Comment on the background quality.
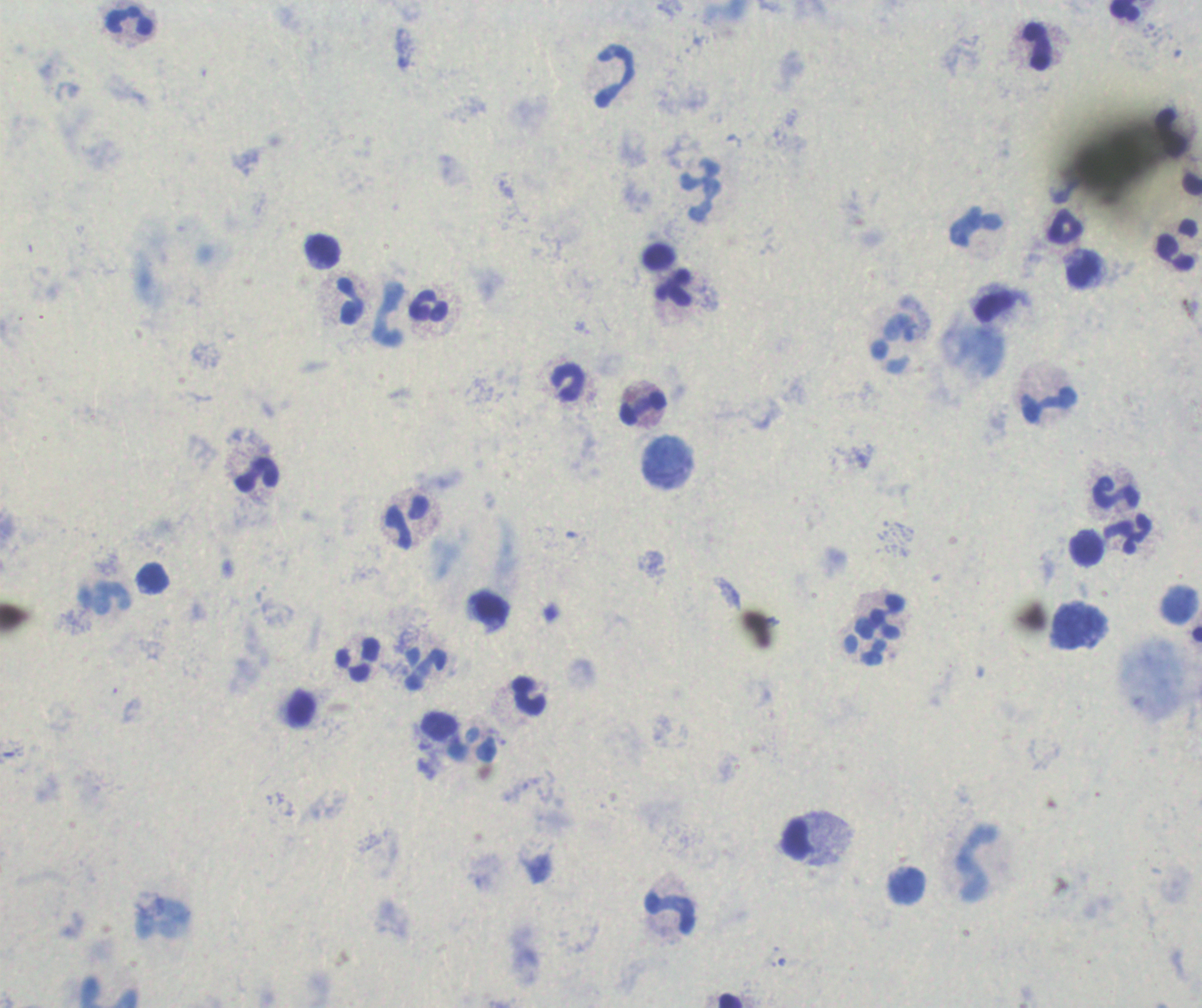
Unsatisfactory.

Approximate centers as {x, y} in pixels. Leukocyte locations: {1125, 11}, {130, 21}, {1038, 47}, {615, 77}, {700, 191}, {1065, 227}, {1177, 246}, {323, 251}, {659, 257}, {1083, 270}, {674, 289}, {349, 301}, {429, 306}, {388, 313}, {568, 382}, {1050, 406}, {643, 408}, {257, 473}, {1117, 493}, {406, 523}, {1128, 536}, {1088, 548}, {103, 600}, {886, 618}, {866, 642}, {358, 662}, {426, 669}, {528, 697}, {301, 708}, {439, 726}, {798, 840}, {975, 863}, {671, 914}. One field from this slide. Result: negative for Plasmodium parasites. Previously used in an actual diagnosis. Romanowsky stain. Image is 1202×1008 pixels. Thick smear of blood. 100x magnification.